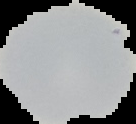

Summary:
  - Preparation: thin blood film
  - Image type: segmented cell region with the area outside set to black
  - Image size: 136×124 pixels
  - Malaria status: uninfected